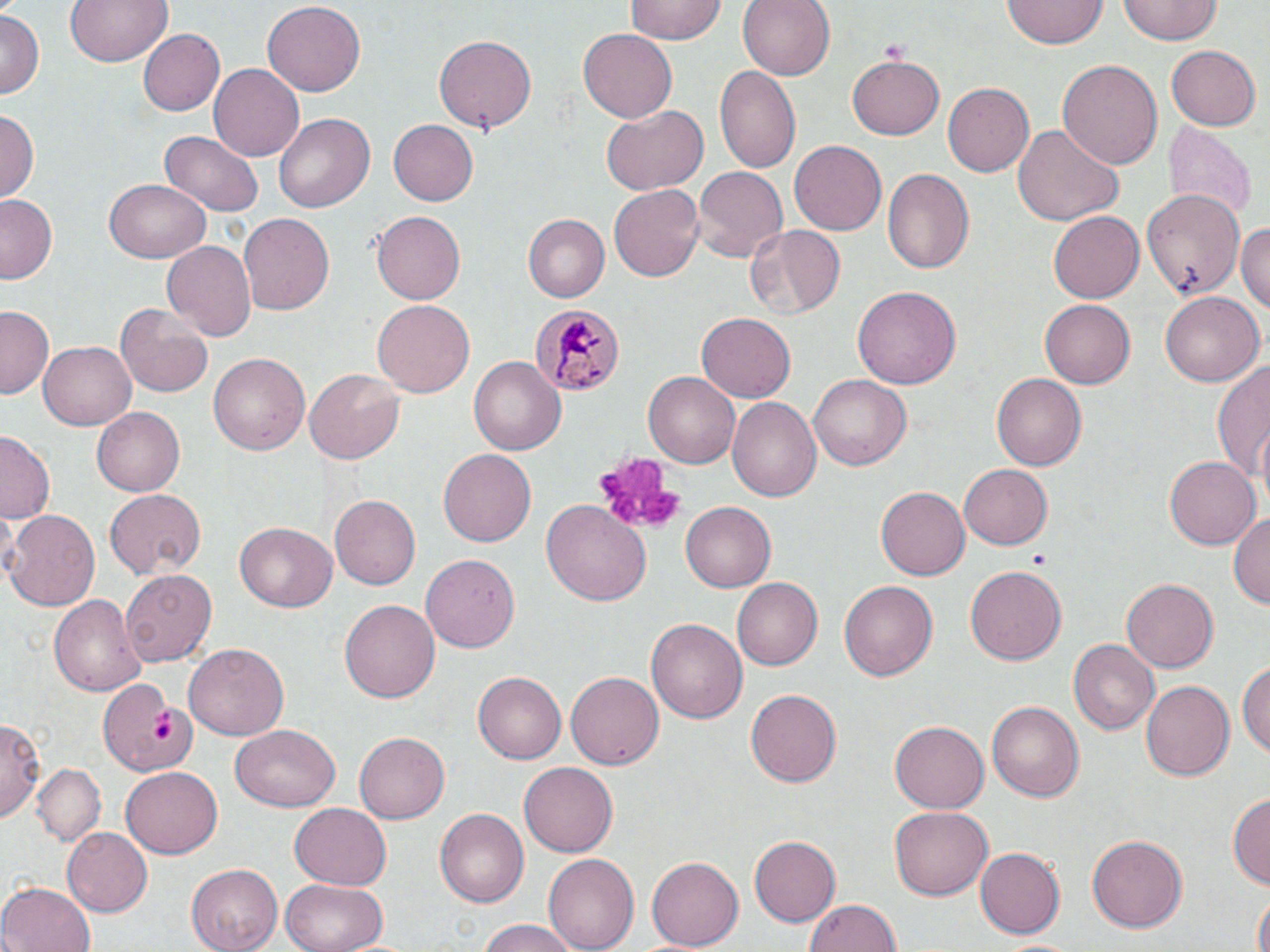
Summary:
  - Coordinate format: approximate bounding boxes as (x1,y1)-(x2,y2) corner pairs in pixels
  - Uninfected red blood cell locations: (65,0)-(173,67), (261,0)-(365,94), (737,0)-(834,81), (1118,0)-(1223,45), (624,1)-(731,44), (1003,1)-(1105,51), (0,12)-(41,98), (136,28)-(226,117), (578,28)-(677,123), (434,34)-(537,134), (1167,46)-(1260,129), (846,55)-(946,140), (1056,59)-(1164,170), (210,64)-(304,160), (713,66)-(801,176), (943,82)-(1034,177), (602,105)-(708,195), (0,109)-(38,205), (273,113)-(375,213), (388,121)-(478,205), (1165,121)-(1257,224), (1012,124)-(1124,227), (159,132)-(265,214), (790,141)-(886,236), (692,168)-(786,266), (883,169)-(974,276), (103,177)-(209,264), (609,183)-(704,284), (1143,192)-(1244,298), (1,195)-(60,284), (371,210)-(466,304), (239,212)-(338,314), (1048,212)-(1143,303), (523,214)-(609,302), (1234,221)-(1270,318), (743,224)-(847,320), (161,239)-(257,344), (853,284)-(962,390), (1160,292)-(1263,385), (1039,298)-(1133,388), (373,300)-(474,399), (114,303)-(214,398), (2,305)-(56,399), (696,312)-(797,403), (39,342)-(136,429), (209,351)-(310,455), (1212,357)-(1270,492), (469,358)-(563,455), (304,368)-(405,466), (643,371)-(740,469), (992,372)-(1086,472), (809,373)-(910,472), (727,396)-(822,503), (91,406)-(184,497), (1,432)-(57,522), (438,449)-(535,547), (1165,456)-(1259,550), (959,461)-(1053,547), (876,487)-(969,581), (103,489)-(206,580), (330,494)-(420,589), (542,499)-(652,609), (680,502)-(776,592), (3,508)-(100,612), (1230,509)-(1269,613), (233,522)-(338,613), (421,551)-(518,650), (120,566)-(216,663), (964,566)-(1068,665), (734,578)-(822,672), (1120,579)-(1217,673), (837,580)-(938,683), (49,591)-(148,697), (339,597)-(438,701), (647,617)-(749,723), (1069,641)-(1158,734), (183,644)-(288,743), (1239,656)-(1270,761), (472,672)-(565,764), (566,672)-(663,773), (99,677)-(200,775), (1141,679)-(1235,783), (746,689)-(844,786), (989,701)-(1084,803), (0,717)-(43,822), (890,722)-(988,812), (231,726)-(342,812), (355,731)-(449,823), (517,760)-(617,854), (32,764)-(106,845), (122,765)-(223,859), (1227,790)-(1270,888), (290,802)-(391,888), (890,807)-(993,900), (435,808)-(530,906), (59,828)-(151,917), (1087,833)-(1187,930), (750,835)-(843,926), (974,848)-(1065,939), (546,852)-(637,952), (645,857)-(742,951), (187,863)-(283,952), (282,876)-(391,952), (0,881)-(96,952), (1252,894)-(1269,952), (803,896)-(902,952), (471,921)-(584,951)
  - Platelet locations: (879,38)-(911,61), (591,453)-(686,538), (1027,551)-(1049,566), (147,709)-(177,744)
  - Plasmodium malariae-infected red blood cell locations: (529,302)-(627,396)
  - Slide-level diagnosis: Plasmodium malariae
  - Field of view: one of a larger specimen
  - Stain: May-Grünwald-Giemsa
  - Image size: 1270×952 pixels
  - Magnification: 1000x
  - Modality: light microscopy
  - Preparation: thin blood film